Assess this cell for malaria.
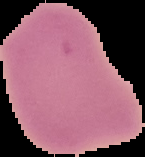

It is uninfected.

Summary:
  - Preparation: thin blood film
  - Image type: segmented cell region on a black background
  - Image size: 145×157 pixels